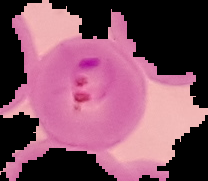

image_type: segmented cell region with the area outside set to black
preparation: thin blood smear
image_size: 208×181 pixels
result: malaria parasites detected